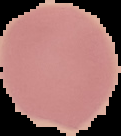
Result: no Plasmodium parasites detected. From a thin blood film. Image is 121×136 pixels. Cell region segmented out of the field of view; the surrounding area is masked to black.